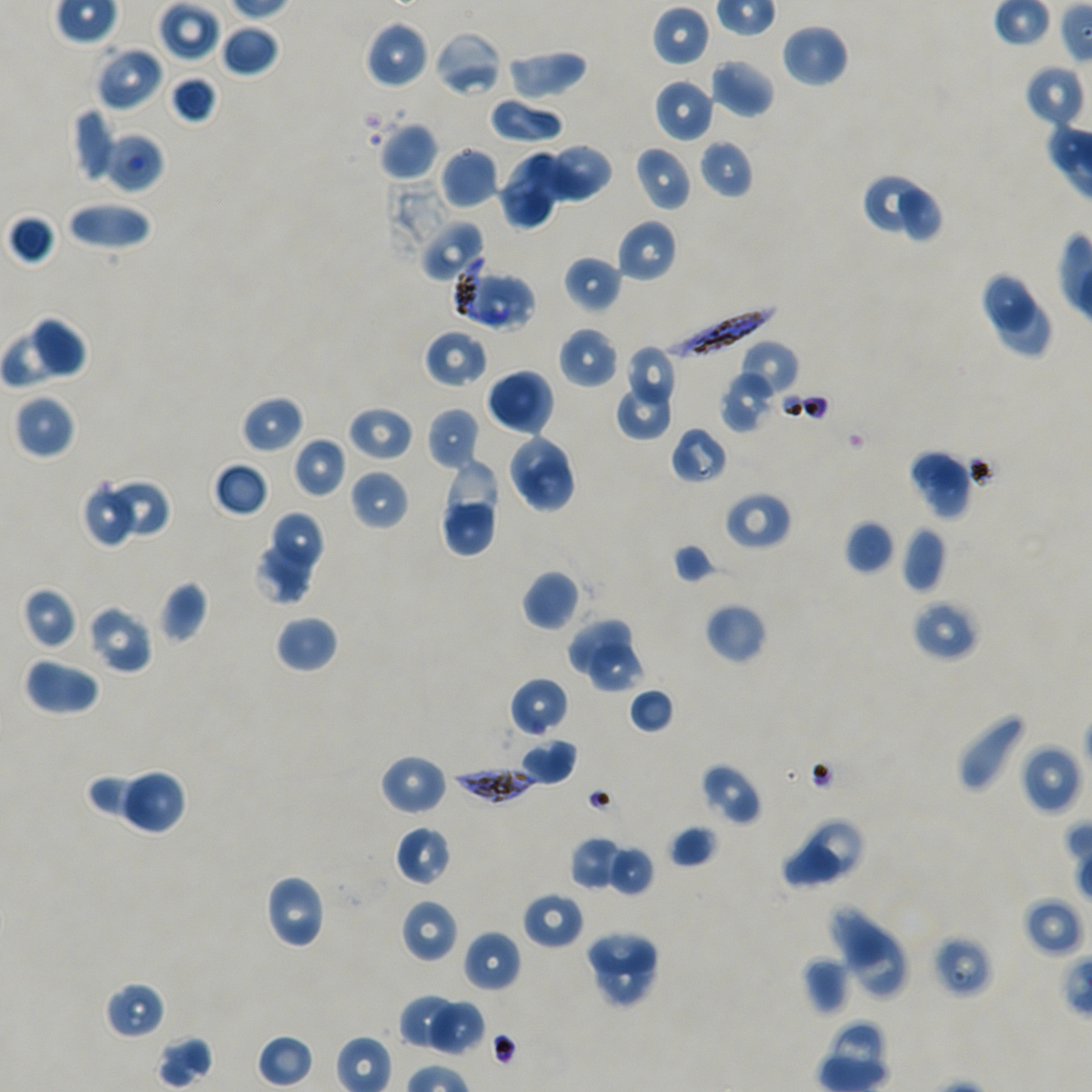
Approximate bounding boxes as {x1, y1, x2, y2} in pixels. Not every red blood cell is marked.
Summary:
  - Locations of red blood cells of indeterminate infection status: {420, 219, 486, 283}, {475, 274, 535, 333}, {930, 934, 994, 999}
  - Locations of infected red blood cells: {454, 256, 487, 323}, {667, 302, 776, 361}, {454, 766, 537, 804}
  - Locations of uninfected red blood cells: {157, 1, 221, 63}, {651, 5, 710, 67}, {363, 20, 429, 90}, {781, 22, 849, 88}, {219, 24, 280, 78}, {433, 30, 503, 98}, {95, 46, 164, 113}, {506, 48, 588, 101}, {709, 57, 775, 118}, {1024, 63, 1087, 129}, {168, 75, 218, 124}, {654, 78, 715, 143}, {488, 96, 564, 145}, {72, 107, 114, 183}, {378, 122, 439, 181}, {99, 132, 164, 194}, {698, 139, 754, 200}, {539, 143, 613, 202}, {634, 145, 693, 213}, {439, 146, 499, 209}, {499, 149, 566, 228}, {860, 172, 926, 232}, {899, 188, 941, 242}, {67, 200, 153, 251}, {7, 214, 57, 266}, {616, 219, 678, 283}, {563, 255, 622, 314}, {979, 270, 1038, 337}, {998, 294, 1052, 359}, {35, 318, 88, 380}, {0, 326, 67, 389}, {558, 326, 619, 389}, {423, 329, 488, 388}, {738, 340, 799, 397}, {624, 344, 676, 403}, {721, 369, 777, 432}, {488, 373, 546, 429}, {615, 385, 674, 441}, {14, 395, 75, 459}, {242, 395, 304, 454}, {347, 405, 414, 462}, {426, 407, 480, 471}, {670, 426, 728, 485}, {505, 431, 569, 500}, {292, 437, 348, 498}, {907, 449, 973, 519}, {520, 458, 575, 513}, {444, 459, 496, 534}, {213, 461, 269, 517}, {349, 469, 410, 531}, {109, 479, 169, 535}, {723, 490, 792, 551}, {83, 492, 133, 548}, {443, 502, 492, 556}, {272, 510, 326, 565}, {843, 520, 896, 574}, {900, 526, 947, 593}, {252, 538, 312, 605}, {672, 542, 723, 584}, {522, 569, 580, 631}, {158, 581, 208, 643}, {21, 586, 79, 650}, {912, 598, 981, 661}, {704, 602, 767, 663}, {87, 604, 153, 674}, {274, 615, 338, 674}, {568, 619, 632, 675}, {587, 644, 644, 692}, {24, 657, 100, 715}, {509, 676, 569, 738}, {627, 687, 674, 734}, {956, 711, 1027, 795}, {519, 738, 577, 785}, {1019, 744, 1082, 816}, {380, 754, 447, 816}, {699, 763, 763, 826}, {117, 769, 187, 835}, {87, 772, 168, 835}, {809, 821, 862, 875}, {395, 824, 452, 886}, {668, 824, 718, 869}, {569, 835, 627, 892}, {779, 840, 840, 890}, {606, 845, 655, 897}, {263, 874, 327, 949}, {522, 892, 584, 951}, {1021, 896, 1085, 958}, {401, 899, 459, 963}, {827, 906, 886, 970}, {844, 924, 907, 996}, {584, 928, 657, 978}, {462, 930, 522, 992}, {598, 951, 649, 1004}, {801, 956, 851, 1015}, {103, 981, 166, 1041}, {398, 994, 473, 1055}, {426, 999, 486, 1055}, {257, 1034, 313, 1088}, {156, 1035, 214, 1089}
  - Objective: 100x, oil immersion, numerical aperture 1.45
  - Donor blood group: A+/O+
  - Field of view: one from this slide
  - Preparation: thin blood film
  - Image size: 1092×1092 pixels
  - Stain: Giemsa
  - Culture: static in-vitro Plasmodium falciparum strain NF54